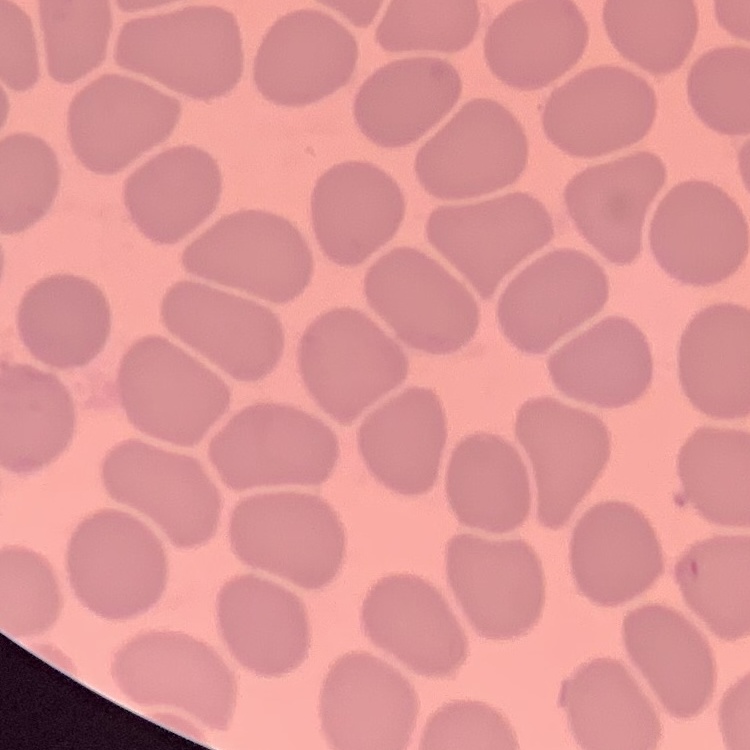
Summary:
  - Erythrocyte morphology: no rouleaux formation
  - Stain: Field's or Giemsa
  - Image type: one tile cut from a larger photomicrograph
  - Preparation: thin blood smear